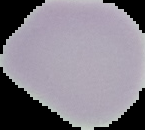
image_size: 145×130 pixels
image_type: cell region segmented out of the field of view; surrounding area masked to black
result: no malaria parasites detected
preparation: thin blood smear